Identify the parasite.
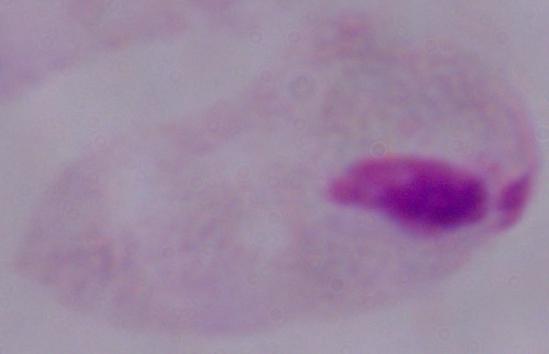

This is a trichomonad.

Captured at 1000x magnification. Photomicrograph.